Report the malaria status of this cell.
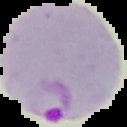

Parasitized.

From a thin blood smear. Cell region segmented out of the field of view; the surrounding area is masked to black. Image is 127×127 pixels.